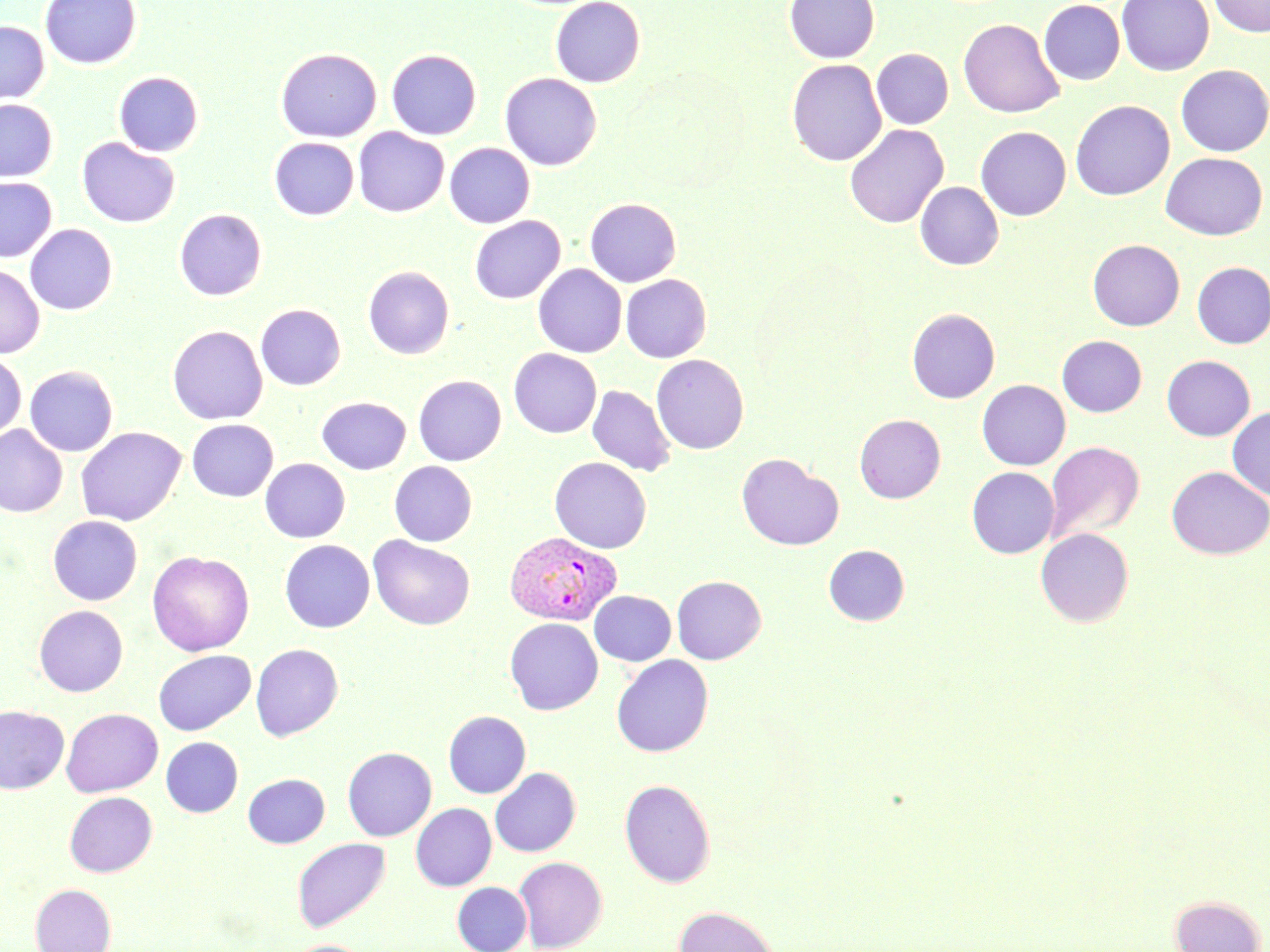

Summary:
  - Coordinate format: approximate bounding boxes as [x1, y1, x2, y2] in pixels
  - Uninfected red blood cell locations: [39, 0, 142, 69], [550, 0, 645, 88], [785, 0, 879, 63], [1039, 0, 1125, 85], [1117, 0, 1214, 76], [1209, 0, 1270, 37], [958, 18, 1065, 118], [0, 21, 49, 104], [276, 48, 382, 142], [871, 48, 953, 129], [386, 49, 482, 140], [787, 59, 886, 166], [1176, 64, 1270, 156], [113, 71, 203, 156], [500, 73, 602, 171], [0, 99, 58, 182], [1070, 100, 1174, 200], [844, 124, 949, 228], [975, 126, 1071, 221], [353, 127, 449, 217], [77, 137, 180, 228], [269, 137, 359, 220], [444, 142, 535, 228], [1160, 152, 1268, 240], [0, 176, 57, 263], [915, 181, 1003, 270], [585, 198, 681, 287], [174, 208, 267, 301], [470, 215, 565, 304], [25, 223, 118, 315], [1088, 239, 1184, 330], [1192, 261, 1270, 348], [0, 263, 45, 358], [533, 264, 627, 357], [363, 265, 455, 359], [621, 274, 712, 362], [255, 303, 346, 390], [907, 308, 1000, 403], [167, 325, 268, 425], [1057, 335, 1147, 417], [509, 348, 601, 438], [0, 350, 27, 444], [651, 354, 749, 454], [1162, 355, 1255, 441], [24, 365, 118, 456], [413, 375, 506, 465], [977, 379, 1071, 470], [587, 385, 676, 477], [316, 396, 411, 474], [1227, 406, 1270, 501], [854, 414, 945, 503], [186, 419, 278, 502], [0, 424, 68, 518], [75, 426, 186, 527], [1044, 441, 1145, 545], [736, 453, 843, 551], [549, 456, 652, 553], [260, 458, 350, 543], [389, 461, 477, 546], [966, 466, 1059, 558], [1166, 466, 1270, 559], [48, 516, 142, 605], [1035, 528, 1134, 627], [368, 535, 475, 631], [279, 539, 375, 632], [823, 544, 910, 626], [147, 551, 255, 656], [671, 575, 766, 664], [589, 590, 676, 666], [34, 605, 128, 696], [504, 617, 603, 715], [250, 644, 343, 741], [153, 650, 255, 736], [611, 655, 714, 757], [0, 705, 69, 794], [61, 708, 163, 797], [443, 711, 531, 798], [161, 736, 243, 817], [342, 746, 437, 841], [489, 767, 581, 857], [243, 773, 330, 848], [619, 778, 716, 888], [64, 792, 157, 876], [410, 802, 497, 891], [291, 838, 391, 932], [514, 856, 608, 952], [452, 881, 532, 952], [30, 883, 116, 952], [1169, 895, 1265, 952], [673, 905, 779, 952], [286, 939, 374, 952]
  - Plasmodium vivax-infected red blood cell locations: [503, 531, 623, 626]
  - Slide-level diagnosis: Plasmodium vivax
  - Stain: May-Grünwald-Giemsa
  - Field of view: single
  - Image size: 1270×952 pixels
  - Modality: light microscopy
  - Magnification: 1000x
  - Preparation: thin blood smear